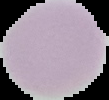
image_size: 109×100 pixels
preparation: thin blood film
image_type: segmented cell region on a black background
result: no malaria parasites seen